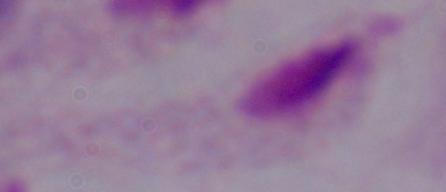

Summary:
  - Modality: micrograph
  - Magnification: 1000x
  - Identification: trichomonad